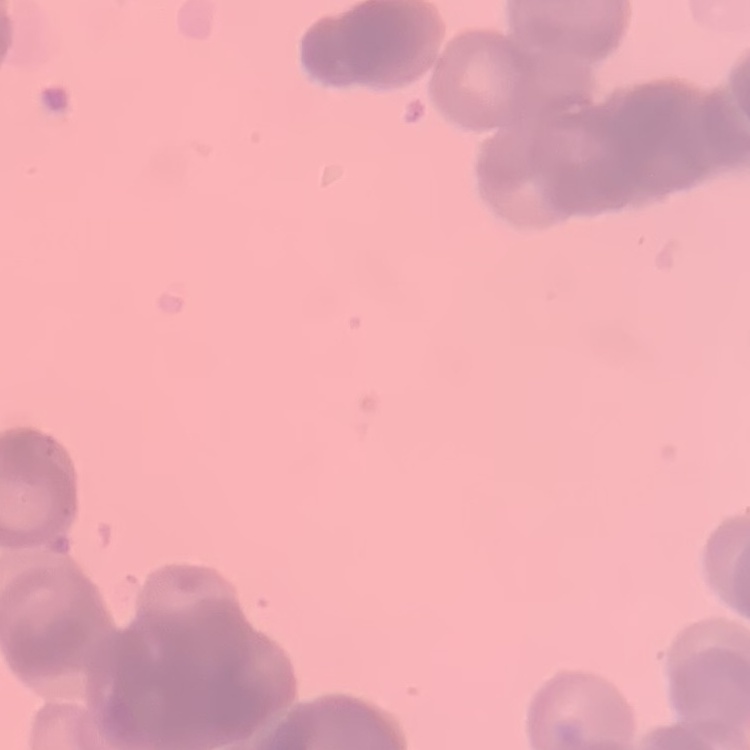
erythrocyte morphology = rouleaux formation
image type = one tile cut from a larger photomicrograph
preparation = thin blood smear
stain = Field's or Giemsa